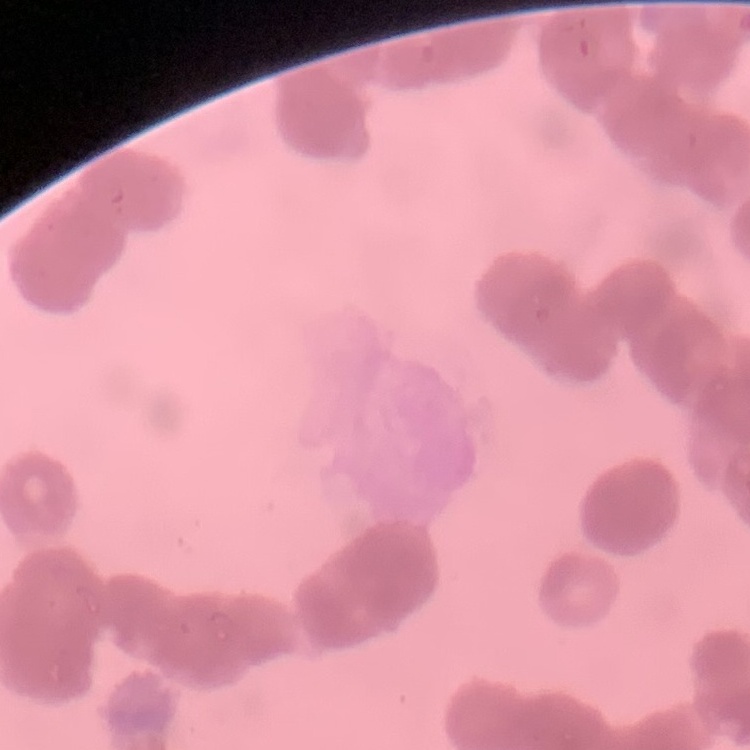

erythrocyte_morphology: rouleaux formation
stain: Field's or Giemsa
image_type: one tile cut from a larger photomicrograph
preparation: thin peripheral smear